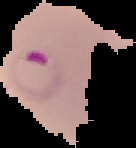

The area outside the segmented cell region is set to black. Image is 136×148 pixels. Result: malaria parasites detected. From a thin blood smear.